Name the blood parasite species.
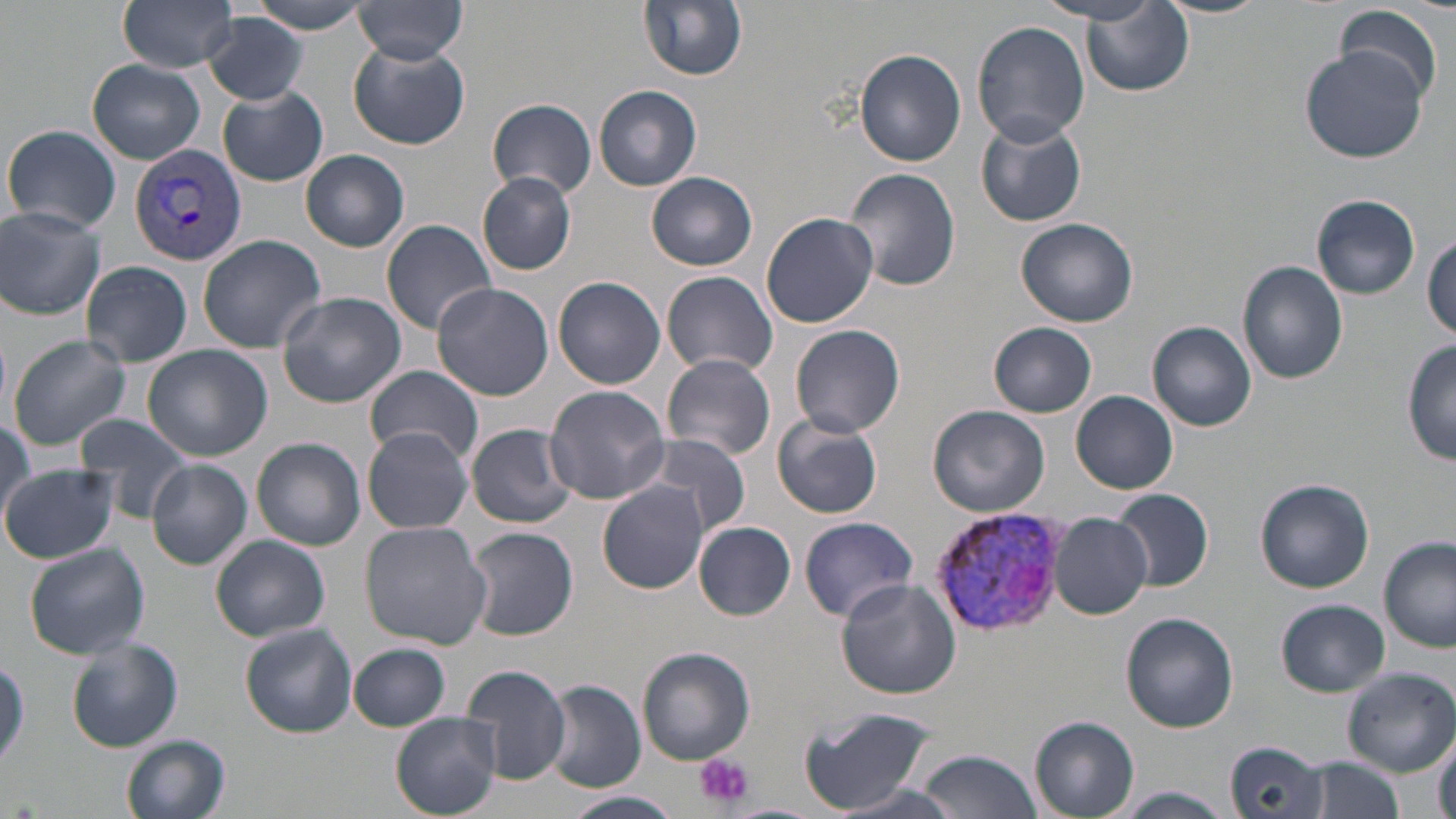
Plasmodium vivax.

Summary:
  - Coordinate format: approximate bounding boxes as (x1, y1, x2, y2) in pixels
  - Plasmodium vivax-infected red blood cell locations: (129, 142, 248, 267), (929, 506, 1071, 635)
  - Uninfected red blood cell locations: (117, 0, 241, 72), (639, 0, 748, 81), (1044, 0, 1170, 25), (1155, 0, 1270, 18), (350, 1, 471, 66), (244, 2, 382, 34), (1080, 4, 1194, 97), (1335, 4, 1446, 107), (202, 13, 309, 106), (972, 21, 1090, 146), (348, 41, 471, 150), (1301, 47, 1428, 164), (853, 48, 968, 167), (85, 58, 205, 165), (594, 85, 702, 191), (219, 87, 327, 185), (488, 99, 597, 199), (975, 115, 1086, 228), (4, 124, 122, 234), (301, 149, 410, 252), (845, 167, 960, 292), (477, 172, 576, 275), (646, 172, 758, 270), (1313, 195, 1420, 300), (1, 208, 106, 319), (761, 211, 880, 328), (1017, 217, 1140, 326), (381, 219, 499, 334), (197, 234, 326, 352), (1425, 234, 1456, 340), (82, 261, 192, 367), (1237, 261, 1350, 384), (662, 271, 777, 378), (552, 275, 667, 389), (431, 282, 553, 400), (276, 291, 406, 408), (550, 302, 664, 464), (1147, 322, 1257, 431), (988, 323, 1097, 418), (789, 325, 906, 439), (7, 334, 132, 450), (1403, 339, 1456, 466), (143, 346, 272, 460), (661, 354, 776, 461), (367, 368, 484, 463), (544, 386, 669, 504), (1071, 390, 1178, 494), (927, 405, 1051, 517), (74, 414, 196, 524), (773, 416, 883, 519), (0, 422, 32, 527), (465, 423, 578, 528), (363, 429, 474, 534), (636, 433, 752, 538), (252, 437, 366, 551), (146, 460, 253, 570), (1, 464, 121, 565), (1255, 477, 1375, 593), (598, 484, 708, 593), (1113, 491, 1214, 590), (1047, 512, 1153, 619), (798, 515, 918, 623), (361, 521, 490, 648), (694, 521, 796, 620), (466, 526, 580, 640), (211, 536, 331, 641), (1381, 536, 1456, 653), (24, 543, 151, 659), (836, 578, 961, 700), (1277, 600, 1389, 695), (1121, 612, 1238, 734), (239, 624, 358, 738), (66, 638, 183, 753), (350, 643, 450, 730), (636, 647, 756, 764), (0, 652, 28, 773), (462, 664, 574, 786), (1343, 669, 1456, 774), (544, 681, 645, 792), (798, 705, 938, 815), (392, 713, 503, 818), (1029, 717, 1140, 817), (1430, 733, 1455, 819), (122, 735, 232, 819), (1225, 740, 1329, 818), (915, 748, 1041, 819), (1305, 758, 1407, 819), (1114, 789, 1234, 819), (556, 791, 685, 819)
  - Platelet locations: (694, 753, 752, 809)
  - Preparation: thin blood film
  - Field of view: one of a larger specimen
  - Magnification: 1000x
  - Modality: light microscopy
  - Image size: 1456×819 pixels
  - Stain: May-Grünwald-Giemsa